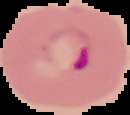

{
  "image_type": "segmented cell region with the area outside set to black",
  "result": "Plasmodium parasites detected",
  "preparation": "thin blood film",
  "image_size": "130×115 pixels"
}